State which parasite is depicted.
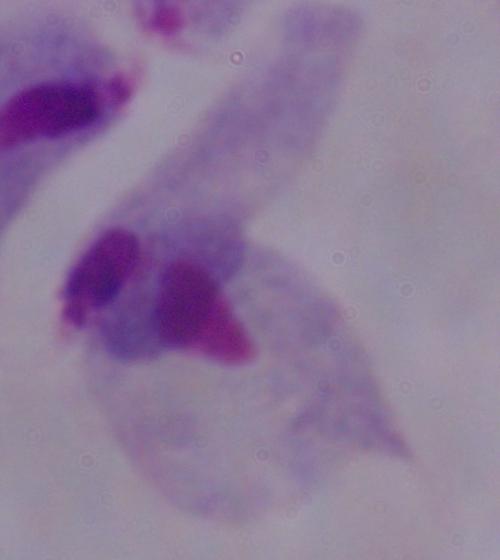
A trichomonad.

magnification = 1000x
modality = photomicrograph